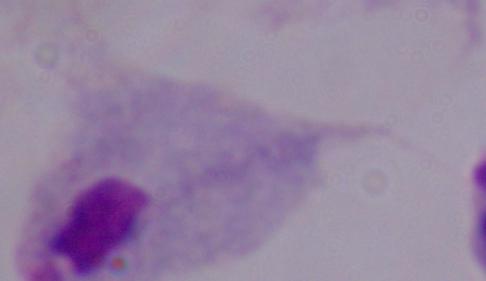
A trichomonad is shown. Captured at 1000x magnification. Photomicrograph.